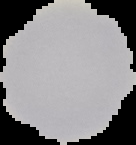

result: no Plasmodium parasites seen
image_size: 136×145 pixels
preparation: thin blood film
image_type: cell region segmented out of the field of view; surrounding area masked to black